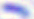
Toxoplasma gondii is seen. 400x magnification. Photomicrograph.